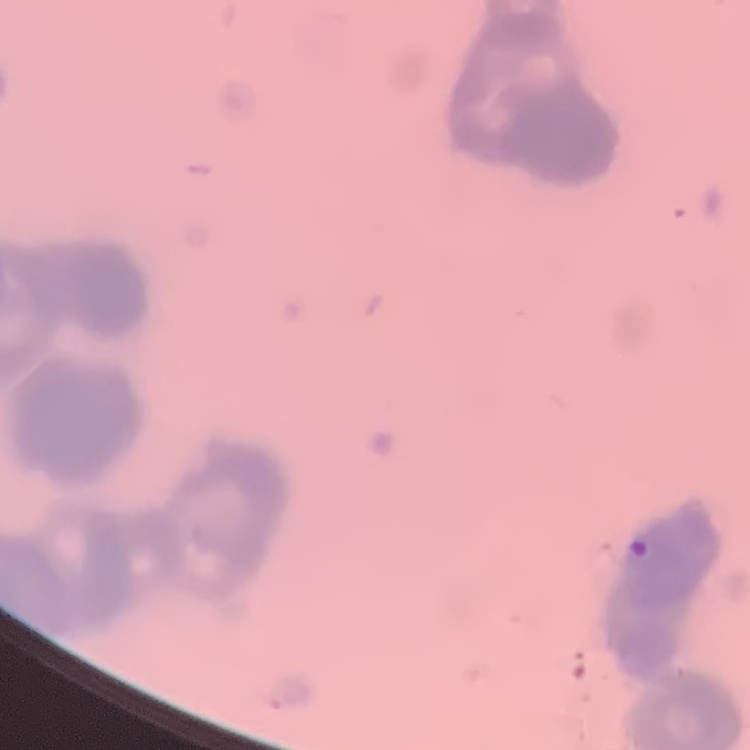

erythrocyte morphology = rouleaux formation
stain = Field's or Giemsa
image type = one tile cut from a larger photomicrograph
preparation = thin blood film